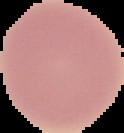

Summary:
  - Image size: 124×133 pixels
  - Result: no Plasmodium parasites detected
  - Image type: cell region segmented out of the field of view; surrounding area masked to black
  - Preparation: thin blood film